Report the malaria status of this cell.
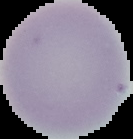

Uninfected.

preparation = thin blood film
image type = segmented cell region on a black background
image size = 133×139 pixels